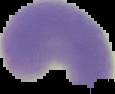

Image is 115×94 pixels. From a thin blood film. Cell region segmented out of the field of view; the surrounding area is masked to black. Malaria status: parasitized.